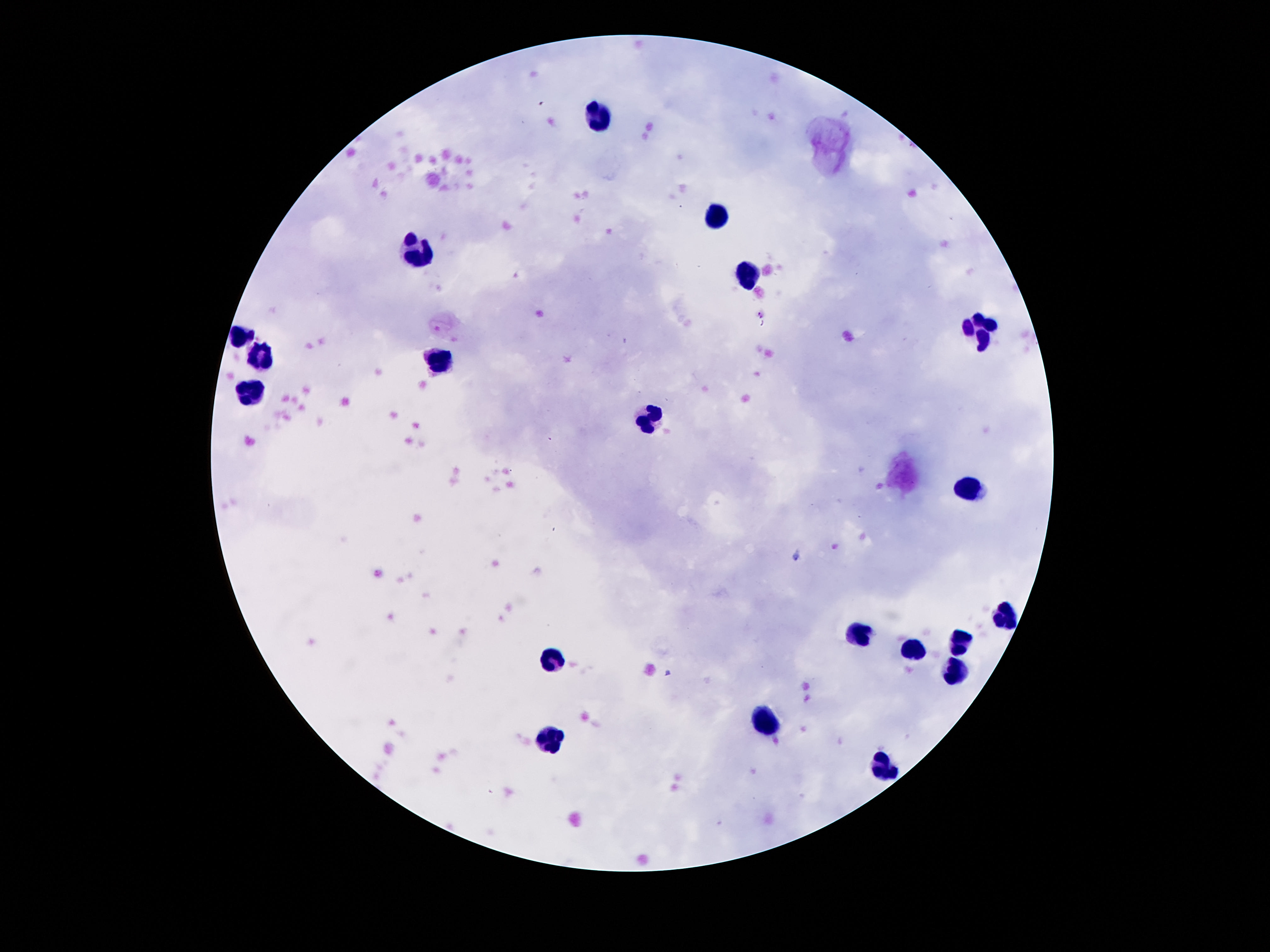
{
  "field_of_view": "single",
  "stain": "Giemsa",
  "magnification": "100x",
  "image_size": "1270×952 pixels",
  "leukocyte_locations": "approximate centers as [x, y] in pixels: [596, 110], [716, 217], [413, 255], [745, 274], [978, 327], [239, 339], [262, 358], [438, 361], [249, 394], [650, 418], [970, 488], [1002, 613], [858, 633], [960, 642], [916, 652], [551, 659], [958, 671], [769, 724], [551, 735], [885, 770]",
  "preparation": "thick peripheral-blood smear",
  "capture": "smartphone camera through the microscope eyepiece",
  "patient_malaria_status": "negative"
}